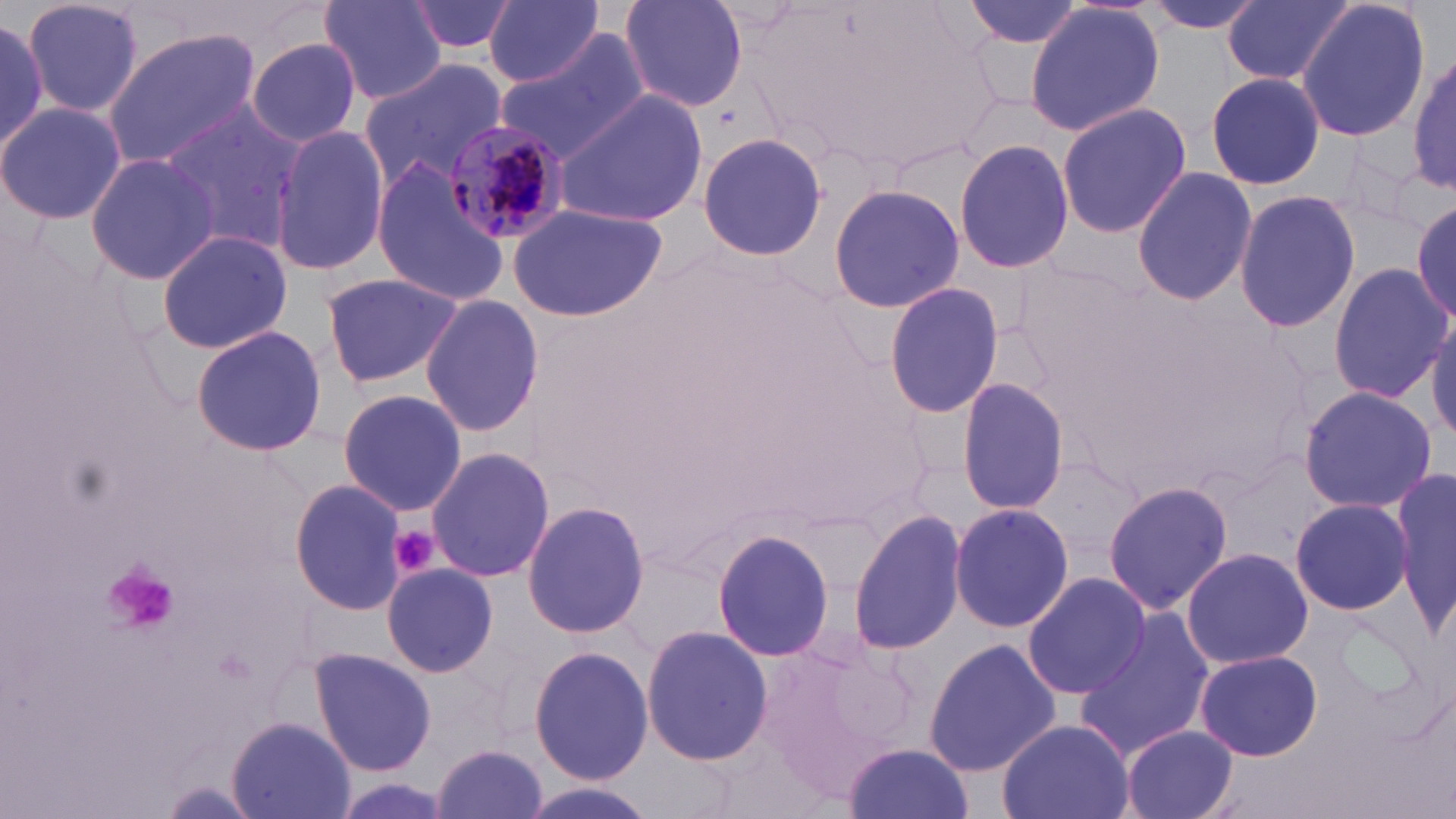
Approximate bounding boxes as (x1,y1)-(x2,y2) corner pairs in pixels. Plasmodium malariae-infected red blood cell locations: (439,118)-(567,246). Uninfected red blood cell locations: (21,0)-(145,120), (321,0)-(446,104), (405,0)-(517,56), (619,0)-(748,113), (958,0)-(1094,50), (1136,0)-(1271,33), (1223,0)-(1353,88), (1294,0)-(1431,144), (481,1)-(609,89), (1023,1)-(1166,137), (0,15)-(50,159), (102,29)-(264,170), (494,34)-(648,165), (245,36)-(363,147), (1410,52)-(1456,195), (358,61)-(511,193), (1204,72)-(1327,192), (553,87)-(707,228), (0,99)-(127,227), (1054,102)-(1192,239), (158,105)-(303,248), (270,124)-(389,279), (697,133)-(829,261), (954,136)-(1073,274), (84,152)-(221,285), (370,156)-(511,308), (1131,167)-(1258,306), (828,184)-(963,314), (1234,190)-(1361,332), (506,202)-(668,321), (1411,202)-(1456,323), (155,230)-(293,354), (1012,253)-(1148,394), (1328,263)-(1450,402), (320,270)-(466,388), (884,279)-(1004,421), (419,295)-(544,437), (1427,314)-(1456,445), (190,324)-(329,457), (956,378)-(1069,516), (1298,384)-(1437,514), (337,388)-(468,517), (425,447)-(555,582), (1391,469)-(1456,637), (288,478)-(410,616), (1103,481)-(1235,614), (1289,496)-(1416,615), (521,498)-(651,640), (950,500)-(1073,633), (848,508)-(969,657), (711,527)-(836,664), (1180,546)-(1313,669), (381,562)-(498,679), (1021,571)-(1150,700), (1071,610)-(1213,760), (640,625)-(774,766), (923,638)-(1062,775), (528,642)-(656,786), (308,647)-(438,777), (1194,649)-(1324,762), (995,717)-(1136,819), (227,718)-(356,819), (1121,727)-(1240,819), (843,742)-(977,819), (431,744)-(551,819), (515,780)-(666,819). Platelet locations: (389,525)-(439,576), (102,568)-(180,635). Slide-level diagnosis: Plasmodium malariae. May-Grünwald-Giemsa-stained preparation. Thin blood film. Single field of view. Light microscopy. Image is 1456×819 pixels. Captured at 1000x magnification.